State the blood parasite species.
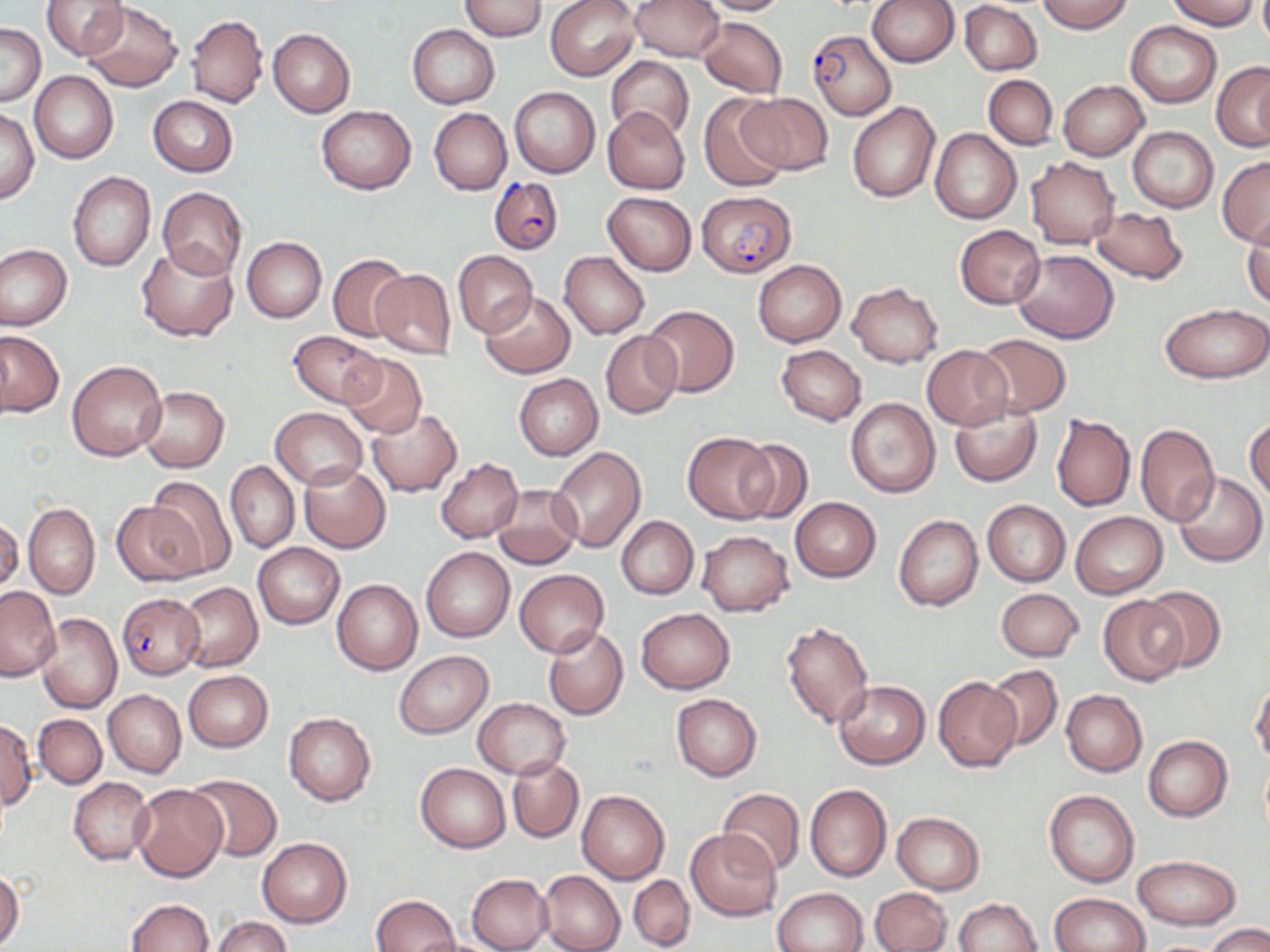
Plasmodium falciparum.

Summary:
  - Coordinate format: approximate bounding boxes as (x1,y1)-(x2,y2) corner pairs in pixels
  - Uninfected red blood cell locations: (39,0)-(127,60), (458,0)-(548,40), (545,0)-(640,81), (629,0)-(723,61), (696,0)-(788,15), (867,0)-(959,67), (1036,0)-(1132,33), (1166,0)-(1259,29), (80,1)-(182,91), (960,2)-(1042,75), (186,15)-(267,108), (697,17)-(787,98), (1127,22)-(1221,106), (1,23)-(45,107), (407,25)-(499,108), (420,26)-(504,192), (268,27)-(355,117), (606,55)-(694,142), (1211,60)-(1270,151), (29,71)-(118,163), (984,75)-(1057,150), (1058,80)-(1148,160), (510,86)-(600,178), (738,92)-(833,174), (699,95)-(790,194), (148,96)-(238,176), (847,102)-(941,203), (1,106)-(39,205), (316,106)-(417,194), (602,106)-(691,194), (429,108)-(512,195), (1128,127)-(1218,213), (930,129)-(1022,225), (1026,156)-(1121,249), (1218,157)-(1270,246), (68,171)-(155,271), (157,187)-(247,280), (603,191)-(697,276), (1089,207)-(1188,282), (1243,216)-(1270,309), (1045,217)-(1183,310), (955,225)-(1045,309), (241,237)-(326,323), (0,244)-(72,331), (136,244)-(238,342), (1012,249)-(1119,344), (453,251)-(537,338), (560,252)-(650,339), (327,254)-(411,343), (752,260)-(846,348), (371,268)-(456,361), (847,281)-(944,368), (479,290)-(575,378), (1160,303)-(1270,384), (643,305)-(740,398), (0,330)-(64,419), (288,330)-(384,408), (599,331)-(682,419), (973,333)-(1073,417), (776,345)-(866,426), (922,346)-(1012,429), (340,354)-(426,439), (67,359)-(168,461), (514,374)-(603,459), (137,386)-(230,472), (845,397)-(941,498), (949,402)-(1043,486), (270,407)-(366,489), (367,409)-(462,497), (1052,413)-(1135,511), (1245,416)-(1270,503), (1134,423)-(1219,526), (682,431)-(778,524), (734,437)-(814,524), (548,446)-(646,553), (435,458)-(522,543), (225,461)-(299,553), (299,462)-(391,553), (1172,471)-(1267,567), (144,475)-(237,578), (492,484)-(582,568), (790,497)-(881,582), (112,498)-(208,586), (982,500)-(1071,587), (23,502)-(100,598), (1070,513)-(1167,598), (894,514)-(983,611), (1,516)-(22,597), (616,516)-(698,599), (697,529)-(794,615), (252,542)-(344,629), (420,546)-(515,642), (514,569)-(608,658), (331,579)-(423,675), (177,581)-(262,672), (1139,584)-(1228,673), (0,585)-(60,680), (994,587)-(1084,662), (1099,595)-(1187,686), (636,608)-(734,693), (35,612)-(122,713), (782,619)-(874,728), (541,627)-(628,720), (393,651)-(492,738), (985,665)-(1062,748), (184,670)-(273,752), (932,676)-(1023,773), (833,680)-(930,769), (1251,683)-(1270,765), (103,689)-(185,778), (1061,690)-(1147,776), (671,693)-(762,781), (472,697)-(570,778), (33,713)-(106,789), (283,713)-(376,805), (0,720)-(37,811), (1143,735)-(1233,821), (507,757)-(582,842), (416,762)-(510,852), (503,764)-(650,851), (186,774)-(282,861), (69,777)-(155,866), (804,782)-(892,883), (130,784)-(228,882), (717,787)-(805,876), (1044,789)-(1139,887), (577,790)-(670,884), (892,812)-(985,894), (687,828)-(782,922), (258,838)-(353,928), (1134,855)-(1240,929), (0,868)-(24,950), (538,870)-(625,952), (467,874)-(553,952), (628,874)-(695,950), (772,887)-(868,952), (871,888)-(951,952), (1050,892)-(1150,952), (372,894)-(459,952), (953,898)-(1042,952), (125,899)-(213,952), (212,916)-(291,952), (1205,923)-(1270,951)
  - Plasmodium falciparum-infected red blood cell locations: (807,30)-(896,119), (488,177)-(563,256), (698,191)-(795,277), (116,593)-(204,678)
  - Image size: 1270×952 pixels
  - Stain: May-Grünwald-Giemsa
  - Magnification: 1000x
  - Field of view: single
  - Modality: light microscopy
  - Preparation: thin blood film